Comment on the morphology of the erythrocytes.
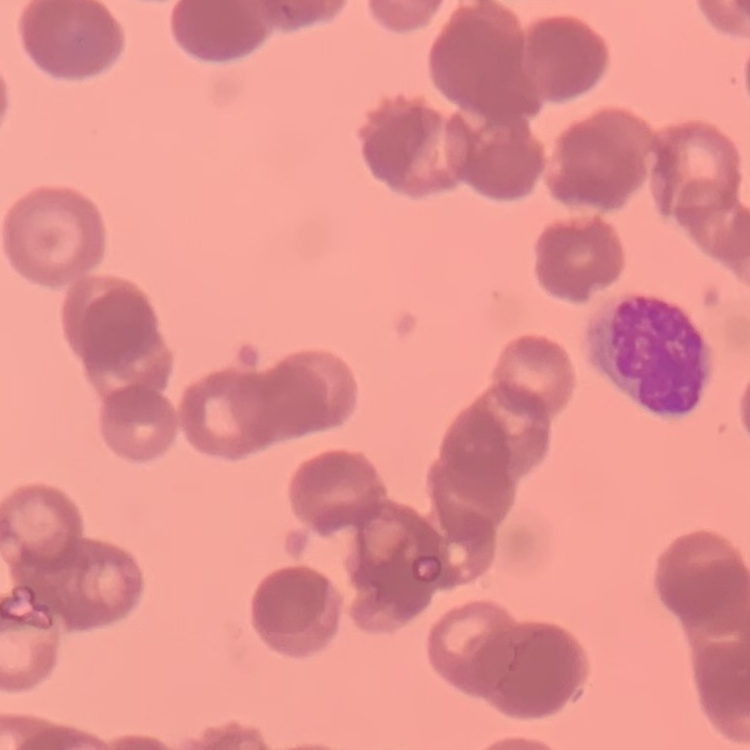

They show rouleaux formation.

Summary:
  - Image type: one tile cut from a larger photomicrograph
  - Stain: Field's or Giemsa
  - Preparation: thin peripheral smear